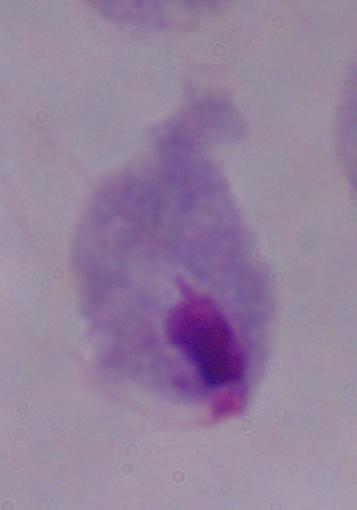

A trichomonad is shown. Micrograph. 1000x magnification.